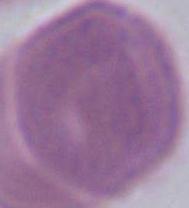

Summary:
  - Modality: photomicrograph
  - Identification: erythrocyte
  - Magnification: 1000x